Mark where platelets are.
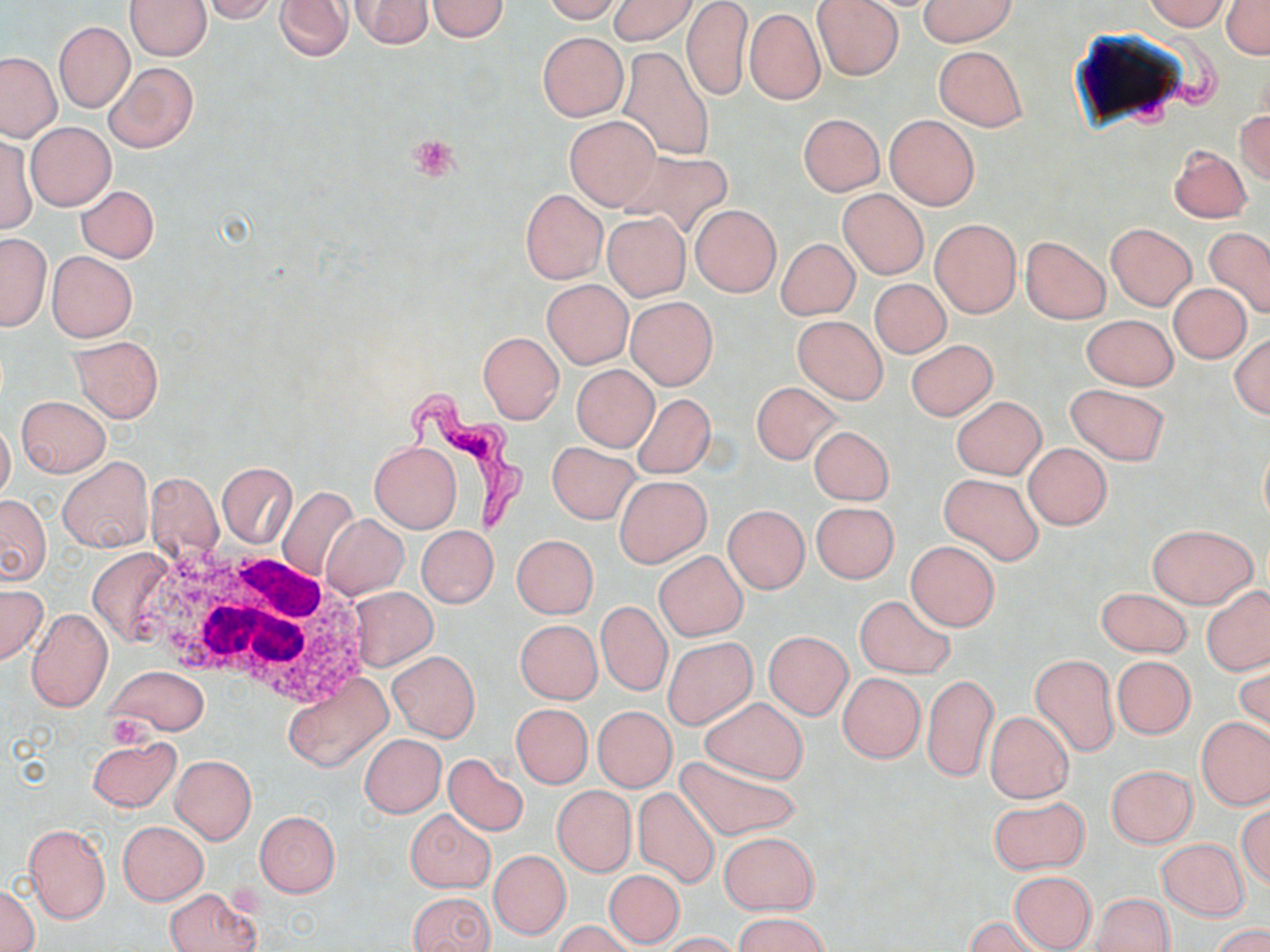

Approximate bounding boxes as named x1/y1/x2/y2 corners in pixels.
Platelets: (x1=409, y1=134, x2=460, y2=183), (x1=104, y1=714, x2=153, y2=750).

Summary:
  - Uninfected red blood cell locations: (x1=125, y1=0, x2=210, y2=59), (x1=204, y1=0, x2=280, y2=23), (x1=275, y1=0, x2=352, y2=61), (x1=541, y1=0, x2=623, y2=23), (x1=607, y1=0, x2=699, y2=46), (x1=681, y1=0, x2=752, y2=102), (x1=813, y1=0, x2=904, y2=80), (x1=918, y1=0, x2=1015, y2=47), (x1=1143, y1=0, x2=1229, y2=30), (x1=1221, y1=0, x2=1270, y2=58), (x1=350, y1=1, x2=434, y2=49), (x1=426, y1=1, x2=509, y2=41), (x1=745, y1=7, x2=825, y2=105), (x1=53, y1=20, x2=134, y2=113), (x1=537, y1=32, x2=628, y2=121), (x1=933, y1=45, x2=1027, y2=132), (x1=616, y1=46, x2=715, y2=160), (x1=0, y1=53, x2=63, y2=143), (x1=104, y1=62, x2=198, y2=153), (x1=1234, y1=108, x2=1270, y2=186), (x1=798, y1=114, x2=885, y2=196), (x1=884, y1=114, x2=980, y2=210), (x1=565, y1=115, x2=660, y2=210), (x1=25, y1=121, x2=115, y2=211), (x1=1, y1=135, x2=37, y2=234), (x1=1169, y1=146, x2=1253, y2=223), (x1=618, y1=148, x2=734, y2=240), (x1=76, y1=185, x2=159, y2=262), (x1=520, y1=189, x2=607, y2=284), (x1=838, y1=189, x2=929, y2=279), (x1=690, y1=205, x2=780, y2=296), (x1=602, y1=213, x2=690, y2=300), (x1=930, y1=219, x2=1021, y2=318), (x1=1105, y1=223, x2=1197, y2=310), (x1=1205, y1=227, x2=1270, y2=318), (x1=0, y1=232, x2=50, y2=332), (x1=1021, y1=236, x2=1112, y2=325), (x1=776, y1=238, x2=860, y2=320), (x1=47, y1=251, x2=137, y2=341), (x1=543, y1=279, x2=633, y2=368), (x1=869, y1=279, x2=950, y2=358), (x1=1168, y1=283, x2=1251, y2=364), (x1=626, y1=296, x2=717, y2=389), (x1=1081, y1=314, x2=1178, y2=390), (x1=792, y1=315, x2=888, y2=404), (x1=478, y1=331, x2=563, y2=424), (x1=1231, y1=333, x2=1270, y2=418), (x1=70, y1=336, x2=163, y2=422), (x1=907, y1=339, x2=997, y2=420), (x1=572, y1=364, x2=658, y2=451), (x1=751, y1=381, x2=842, y2=465), (x1=1065, y1=383, x2=1170, y2=466), (x1=632, y1=393, x2=715, y2=479), (x1=16, y1=395, x2=111, y2=478), (x1=951, y1=395, x2=1045, y2=479), (x1=0, y1=418, x2=15, y2=502), (x1=809, y1=425, x2=895, y2=505), (x1=547, y1=441, x2=641, y2=524), (x1=370, y1=442, x2=461, y2=532), (x1=1022, y1=443, x2=1112, y2=530), (x1=57, y1=456, x2=153, y2=552), (x1=218, y1=463, x2=296, y2=548), (x1=145, y1=471, x2=225, y2=563), (x1=939, y1=472, x2=1043, y2=565), (x1=615, y1=475, x2=711, y2=568), (x1=276, y1=485, x2=360, y2=581), (x1=0, y1=494, x2=51, y2=585), (x1=811, y1=502, x2=899, y2=583), (x1=723, y1=504, x2=809, y2=593), (x1=321, y1=514, x2=409, y2=599), (x1=1146, y1=523, x2=1257, y2=608), (x1=416, y1=526, x2=498, y2=608), (x1=511, y1=534, x2=598, y2=618), (x1=906, y1=542, x2=1000, y2=630), (x1=86, y1=547, x2=178, y2=647), (x1=654, y1=550, x2=748, y2=641), (x1=0, y1=583, x2=45, y2=665), (x1=346, y1=586, x2=438, y2=670), (x1=1202, y1=586, x2=1270, y2=675), (x1=1097, y1=588, x2=1193, y2=658), (x1=854, y1=595, x2=954, y2=677), (x1=597, y1=601, x2=672, y2=696), (x1=26, y1=607, x2=112, y2=712), (x1=515, y1=620, x2=602, y2=703), (x1=763, y1=632, x2=852, y2=721), (x1=663, y1=637, x2=757, y2=728), (x1=389, y1=651, x2=480, y2=741), (x1=1030, y1=654, x2=1119, y2=756), (x1=1112, y1=656, x2=1195, y2=739), (x1=1235, y1=661, x2=1269, y2=742), (x1=108, y1=664, x2=206, y2=735), (x1=284, y1=672, x2=391, y2=774), (x1=838, y1=673, x2=925, y2=763), (x1=922, y1=673, x2=997, y2=782), (x1=699, y1=697, x2=808, y2=784), (x1=511, y1=704, x2=592, y2=788), (x1=593, y1=706, x2=677, y2=791), (x1=984, y1=711, x2=1074, y2=803), (x1=1197, y1=717, x2=1269, y2=811), (x1=360, y1=734, x2=446, y2=818), (x1=86, y1=737, x2=181, y2=813), (x1=442, y1=753, x2=530, y2=836), (x1=171, y1=755, x2=256, y2=843), (x1=673, y1=755, x2=803, y2=842), (x1=1106, y1=765, x2=1197, y2=848), (x1=552, y1=786, x2=636, y2=876), (x1=633, y1=786, x2=719, y2=890), (x1=988, y1=796, x2=1090, y2=875), (x1=1237, y1=804, x2=1270, y2=889), (x1=406, y1=810, x2=494, y2=893), (x1=255, y1=811, x2=340, y2=897), (x1=117, y1=820, x2=208, y2=905), (x1=24, y1=824, x2=111, y2=924), (x1=719, y1=832, x2=818, y2=915), (x1=1157, y1=839, x2=1250, y2=920), (x1=489, y1=850, x2=570, y2=938), (x1=604, y1=869, x2=684, y2=948), (x1=1008, y1=871, x2=1096, y2=951), (x1=2, y1=882, x2=39, y2=951), (x1=165, y1=887, x2=261, y2=952), (x1=406, y1=891, x2=496, y2=952), (x1=1093, y1=893, x2=1174, y2=952), (x1=735, y1=913, x2=832, y2=952), (x1=964, y1=916, x2=1049, y2=952), (x1=555, y1=920, x2=635, y2=952), (x1=1212, y1=924, x2=1269, y2=952), (x1=660, y1=931, x2=745, y2=951)
  - White blood cell locations: (x1=138, y1=547, x2=368, y2=699)
  - Trypanosoma brucei locations: (x1=389, y1=393, x2=531, y2=540)
  - Slide-level diagnosis: Trypanosoma brucei
  - Image size: 1270×952 pixels
  - Preparation: thin blood film
  - Stain: May-Grünwald-Giemsa
  - Modality: optical microscopy
  - Magnification: 1000x
  - Field of view: single